Assess this cell for malaria.
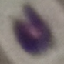

Uninfected.

preparation = thin blood film
image type = cell patch, automatically extracted from a larger field of view and resized to 64 × 64 pixels
capture = smartphone camera at the microscope eyepiece
stain = Giemsa